Point out each malaria parasite.
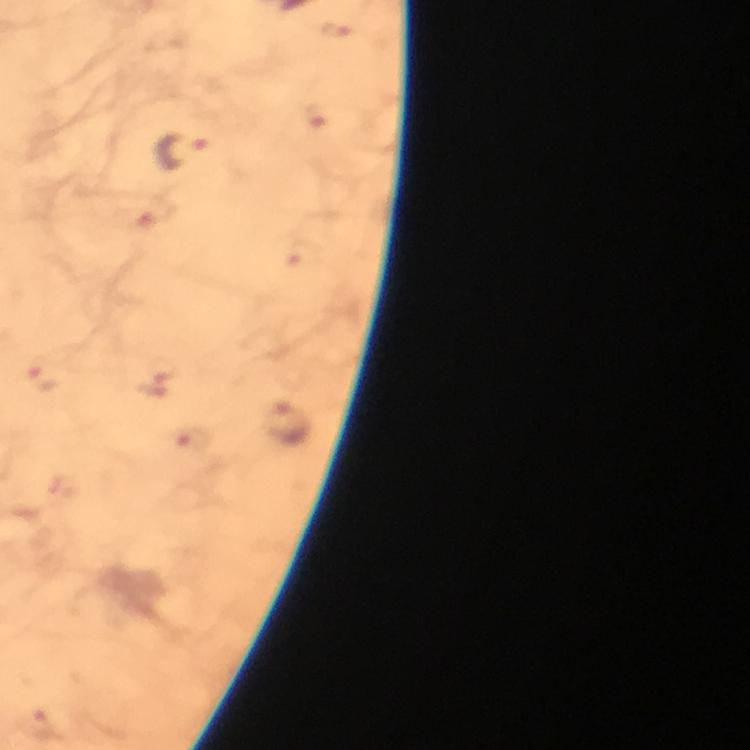
Approximate centers as {x, y} in pixels.
Malaria parasites: {338, 31}, {316, 116}, {182, 151}, {161, 375}, {43, 377}, {287, 424}, {195, 440}.

Image is 750×750 pixels. From a malaria diagnostic workup. Thick blood film. Cropped region of a single field of view. Photographed with a smartphone mounted on the microscope. 100x magnification. Giemsa-stained preparation. Immersion oil applied.